Report the malaria status of this cell.
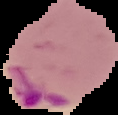
Parasitized.

Segmented cell region on a black background. From a thin blood film. Image is 118×115 pixels.